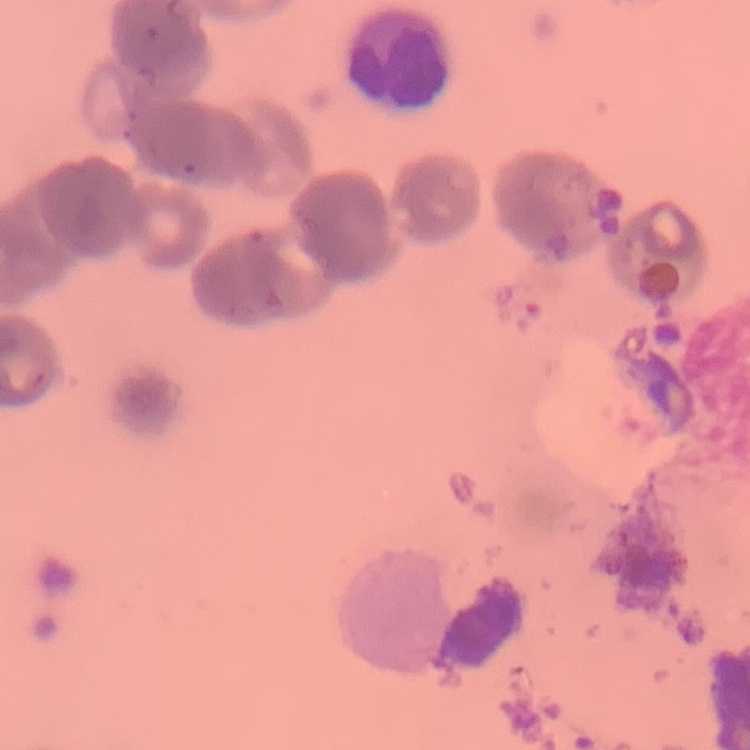

red blood cell morphology = rouleaux formation
image type = square crop of a larger photomicrograph
stain = Field's or Giemsa
preparation = thin blood smear